Assess this cell for malaria.
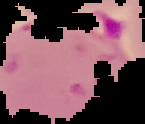
It is parasitized.

Summary:
  - Preparation: thin blood film
  - Image size: 145×124 pixels
  - Image type: segmented cell region on a black background